State the preparation type.
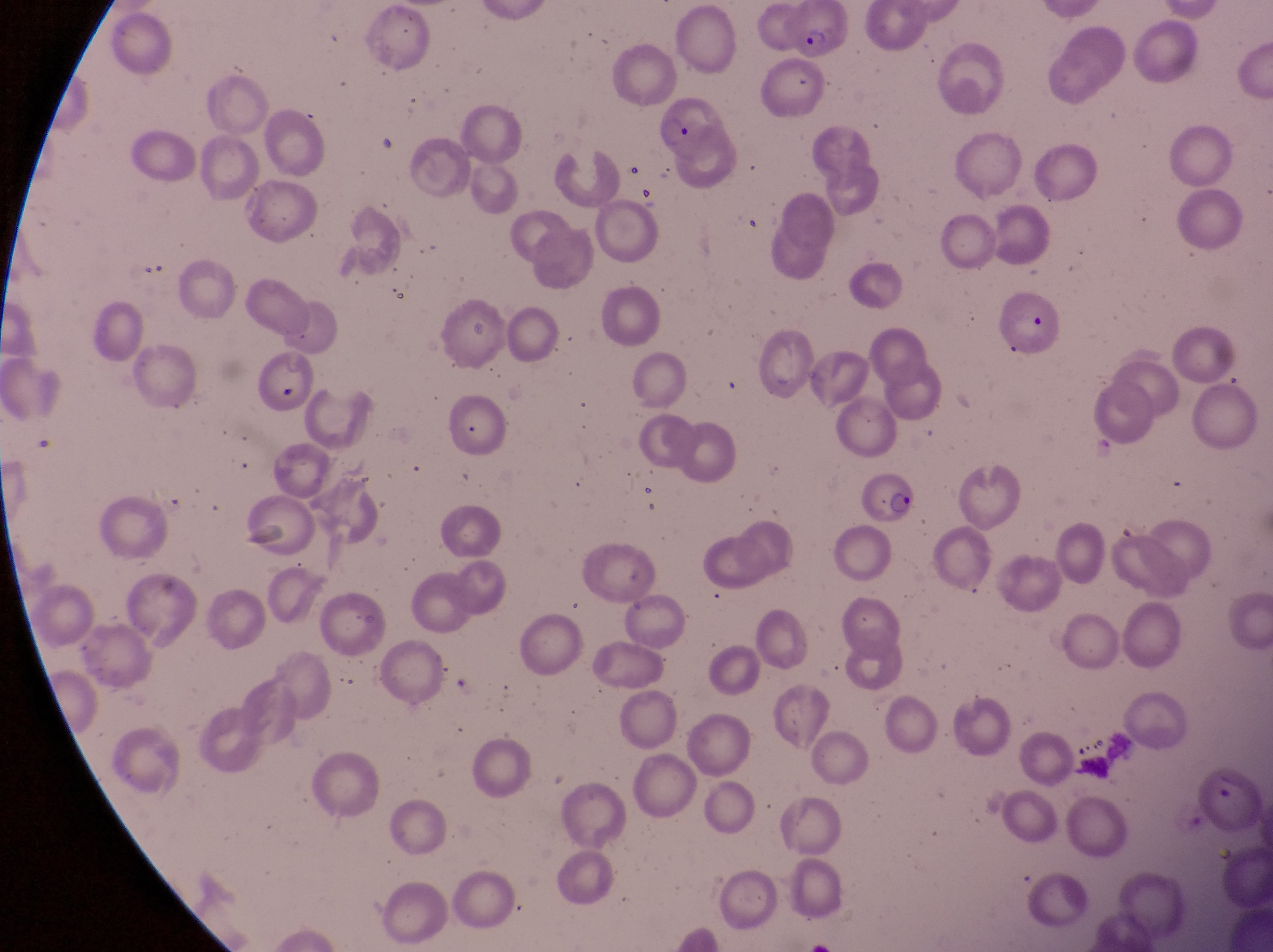

This is a thin smear.

Approximate bounding boxes as left top right bottom in pixels. Leukocyte locations: 1076 727 1139 792. Parasitised red blood cell locations: 789 3 852 56; 656 93 723 167; 1001 280 1064 362; 859 469 917 527; 1195 761 1264 838. Photographed through the eyepiece of an Olympus CX-23 microscope with a smartphone camera. Sample from Uganda. Magnification of 1000x. Single field of view. Image is 1273×952 pixels.